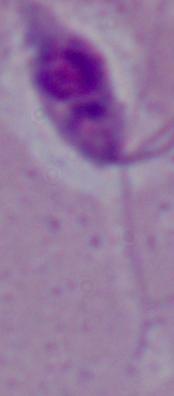

Micrograph. 1000x magnification. A Leishmania parasite is shown.